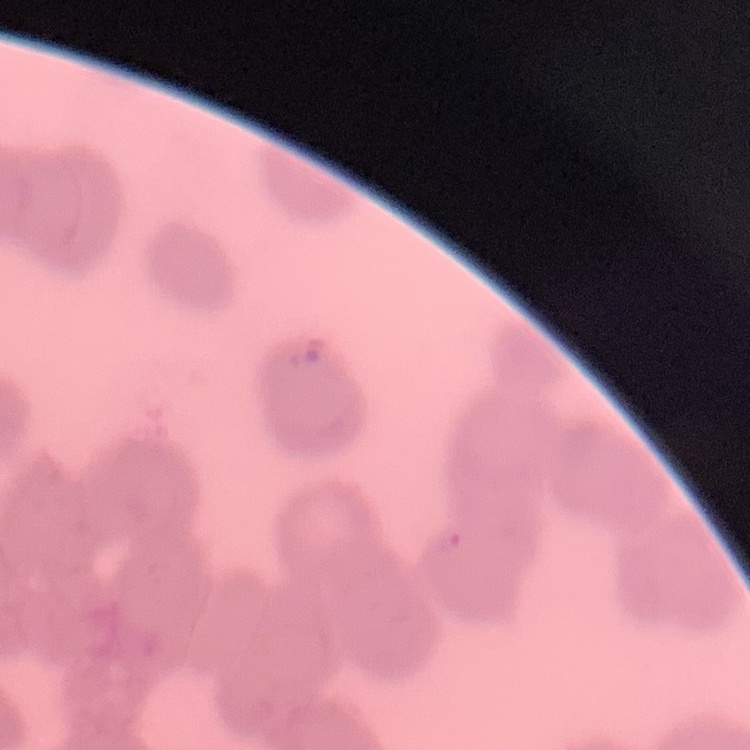
Summary:
  - Erythrocyte morphology: rouleaux formation
  - Stain: Field's or Giemsa
  - Image type: one tile cut from a larger photomicrograph
  - Preparation: thin peripheral smear